Locate every Plasmodium falciparum-infected red blood cell.
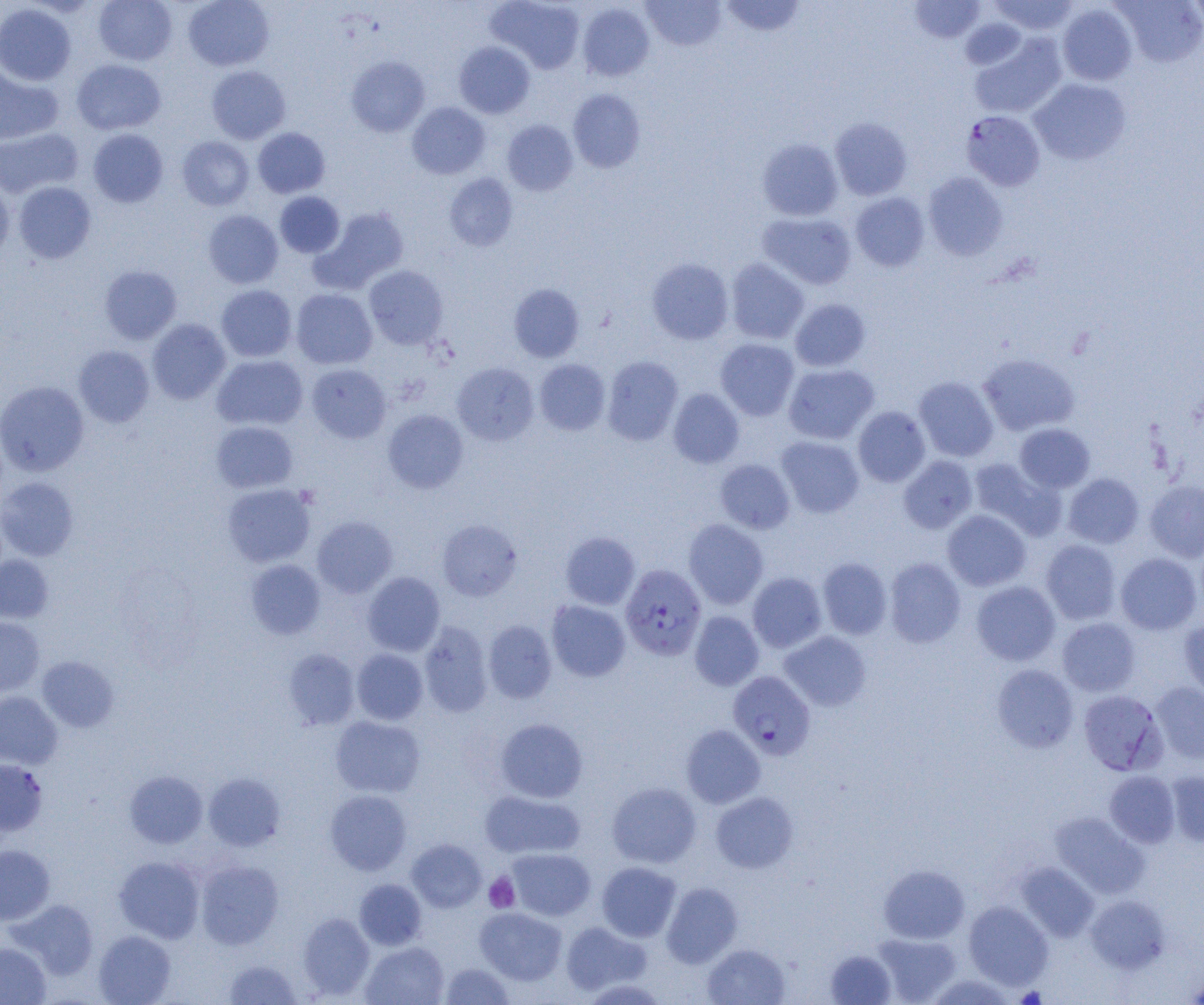

Approximate bounding boxes as named x1/y1/x2/y2 corners in pixels.
Plasmodium falciparum-infected red blood cells: (x1=961, y1=110, x2=1045, y2=191), (x1=620, y1=564, x2=706, y2=660), (x1=728, y1=671, x2=815, y2=760), (x1=1078, y1=690, x2=1167, y2=775).

Platelet locations: (x1=484, y1=873, x2=519, y2=912). Uninfected red blood cell locations: (x1=93, y1=0, x2=177, y2=65), (x1=183, y1=0, x2=274, y2=71), (x1=487, y1=0, x2=585, y2=73), (x1=641, y1=0, x2=726, y2=50), (x1=719, y1=0, x2=806, y2=38), (x1=989, y1=0, x2=1080, y2=36), (x1=909, y1=1, x2=985, y2=43), (x1=1114, y1=1, x2=1204, y2=67), (x1=1187, y1=1, x2=1204, y2=33), (x1=0, y1=3, x2=76, y2=85), (x1=577, y1=3, x2=654, y2=81), (x1=1057, y1=3, x2=1138, y2=86), (x1=960, y1=17, x2=1026, y2=70), (x1=970, y1=33, x2=1067, y2=119), (x1=454, y1=41, x2=535, y2=118), (x1=346, y1=56, x2=430, y2=137), (x1=72, y1=59, x2=166, y2=135), (x1=206, y1=65, x2=291, y2=144), (x1=0, y1=66, x2=62, y2=145), (x1=1029, y1=78, x2=1131, y2=165), (x1=567, y1=89, x2=645, y2=173), (x1=407, y1=102, x2=490, y2=179), (x1=830, y1=117, x2=912, y2=200), (x1=502, y1=120, x2=578, y2=195), (x1=252, y1=127, x2=330, y2=198), (x1=0, y1=128, x2=82, y2=198), (x1=88, y1=129, x2=168, y2=208), (x1=176, y1=136, x2=254, y2=210), (x1=757, y1=138, x2=843, y2=221), (x1=444, y1=172, x2=518, y2=251), (x1=924, y1=172, x2=1007, y2=261), (x1=0, y1=180, x2=14, y2=262), (x1=14, y1=181, x2=96, y2=263), (x1=275, y1=191, x2=345, y2=258), (x1=850, y1=192, x2=929, y2=271), (x1=312, y1=207, x2=409, y2=292), (x1=203, y1=210, x2=283, y2=289), (x1=757, y1=212, x2=857, y2=290), (x1=647, y1=258, x2=734, y2=345), (x1=725, y1=258, x2=809, y2=344), (x1=99, y1=265, x2=182, y2=344), (x1=364, y1=265, x2=449, y2=349), (x1=508, y1=283, x2=584, y2=362), (x1=216, y1=285, x2=297, y2=362), (x1=291, y1=289, x2=377, y2=369), (x1=790, y1=298, x2=871, y2=372), (x1=147, y1=319, x2=231, y2=404), (x1=715, y1=338, x2=799, y2=420), (x1=73, y1=345, x2=155, y2=427), (x1=978, y1=353, x2=1080, y2=436), (x1=211, y1=354, x2=308, y2=430), (x1=602, y1=356, x2=683, y2=445), (x1=535, y1=359, x2=610, y2=435), (x1=452, y1=362, x2=539, y2=445), (x1=783, y1=363, x2=879, y2=444), (x1=306, y1=364, x2=391, y2=444), (x1=913, y1=376, x2=999, y2=462), (x1=0, y1=381, x2=89, y2=476), (x1=668, y1=389, x2=744, y2=468), (x1=853, y1=406, x2=931, y2=487), (x1=382, y1=409, x2=469, y2=493), (x1=211, y1=421, x2=298, y2=493), (x1=1015, y1=423, x2=1095, y2=493), (x1=776, y1=436, x2=864, y2=518), (x1=898, y1=455, x2=977, y2=533), (x1=968, y1=458, x2=1065, y2=540), (x1=715, y1=459, x2=795, y2=533), (x1=1063, y1=473, x2=1144, y2=548), (x1=0, y1=477, x2=79, y2=561), (x1=1144, y1=480, x2=1204, y2=562), (x1=222, y1=483, x2=316, y2=567), (x1=942, y1=510, x2=1031, y2=591), (x1=312, y1=516, x2=397, y2=598), (x1=437, y1=519, x2=521, y2=601), (x1=683, y1=519, x2=769, y2=609), (x1=560, y1=531, x2=640, y2=610), (x1=1040, y1=539, x2=1121, y2=624), (x1=1115, y1=553, x2=1202, y2=635), (x1=0, y1=555, x2=53, y2=623), (x1=818, y1=557, x2=892, y2=639), (x1=885, y1=558, x2=966, y2=647), (x1=245, y1=559, x2=325, y2=640), (x1=362, y1=572, x2=445, y2=656), (x1=747, y1=572, x2=828, y2=653), (x1=971, y1=581, x2=1060, y2=666), (x1=546, y1=600, x2=630, y2=681), (x1=689, y1=611, x2=763, y2=690), (x1=1179, y1=616, x2=1204, y2=700), (x1=0, y1=617, x2=45, y2=696), (x1=1057, y1=618, x2=1141, y2=696), (x1=483, y1=620, x2=557, y2=703), (x1=418, y1=621, x2=493, y2=717), (x1=779, y1=631, x2=871, y2=711), (x1=283, y1=648, x2=360, y2=730), (x1=351, y1=648, x2=428, y2=725), (x1=37, y1=656, x2=119, y2=732), (x1=992, y1=664, x2=1078, y2=752), (x1=1151, y1=682, x2=1204, y2=764), (x1=0, y1=691, x2=62, y2=769), (x1=330, y1=715, x2=425, y2=798), (x1=495, y1=718, x2=588, y2=802), (x1=681, y1=724, x2=765, y2=808), (x1=0, y1=759, x2=48, y2=836), (x1=124, y1=770, x2=207, y2=848), (x1=1165, y1=770, x2=1204, y2=846), (x1=1104, y1=771, x2=1180, y2=848), (x1=203, y1=772, x2=285, y2=851), (x1=607, y1=781, x2=701, y2=868), (x1=325, y1=789, x2=412, y2=875), (x1=479, y1=790, x2=585, y2=860), (x1=710, y1=791, x2=798, y2=873), (x1=1049, y1=812, x2=1149, y2=898), (x1=406, y1=839, x2=486, y2=912), (x1=0, y1=845, x2=54, y2=924), (x1=506, y1=848, x2=596, y2=921), (x1=113, y1=856, x2=205, y2=943), (x1=196, y1=860, x2=283, y2=949), (x1=596, y1=861, x2=681, y2=942), (x1=1015, y1=862, x2=1100, y2=941), (x1=878, y1=864, x2=970, y2=943), (x1=354, y1=878, x2=426, y2=950), (x1=661, y1=882, x2=742, y2=968), (x1=1086, y1=894, x2=1170, y2=974), (x1=8, y1=899, x2=99, y2=979), (x1=963, y1=901, x2=1053, y2=989), (x1=475, y1=907, x2=567, y2=985), (x1=298, y1=912, x2=375, y2=999), (x1=561, y1=921, x2=650, y2=996), (x1=93, y1=930, x2=176, y2=1004), (x1=871, y1=932, x2=961, y2=1004), (x1=360, y1=942, x2=449, y2=1005), (x1=0, y1=943, x2=51, y2=1004), (x1=702, y1=943, x2=791, y2=1005), (x1=825, y1=948, x2=896, y2=1004), (x1=224, y1=958, x2=302, y2=1004), (x1=440, y1=962, x2=514, y2=1005), (x1=1187, y1=971, x2=1204, y2=1004), (x1=926, y1=973, x2=1018, y2=1005). Slide-level diagnosis: Plasmodium falciparum. Image is 1204×1005 pixels. Single field of view. 1000x magnification. Optical microscopy. Thin blood film.